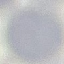 Result: negative for malaria parasites. Giemsa stain. Thin smear of blood. Photographed with a smartphone camera at the microscope eyepiece. Cell patch, automatically extracted from a larger field of view and resized to 64 × 64 pixels.